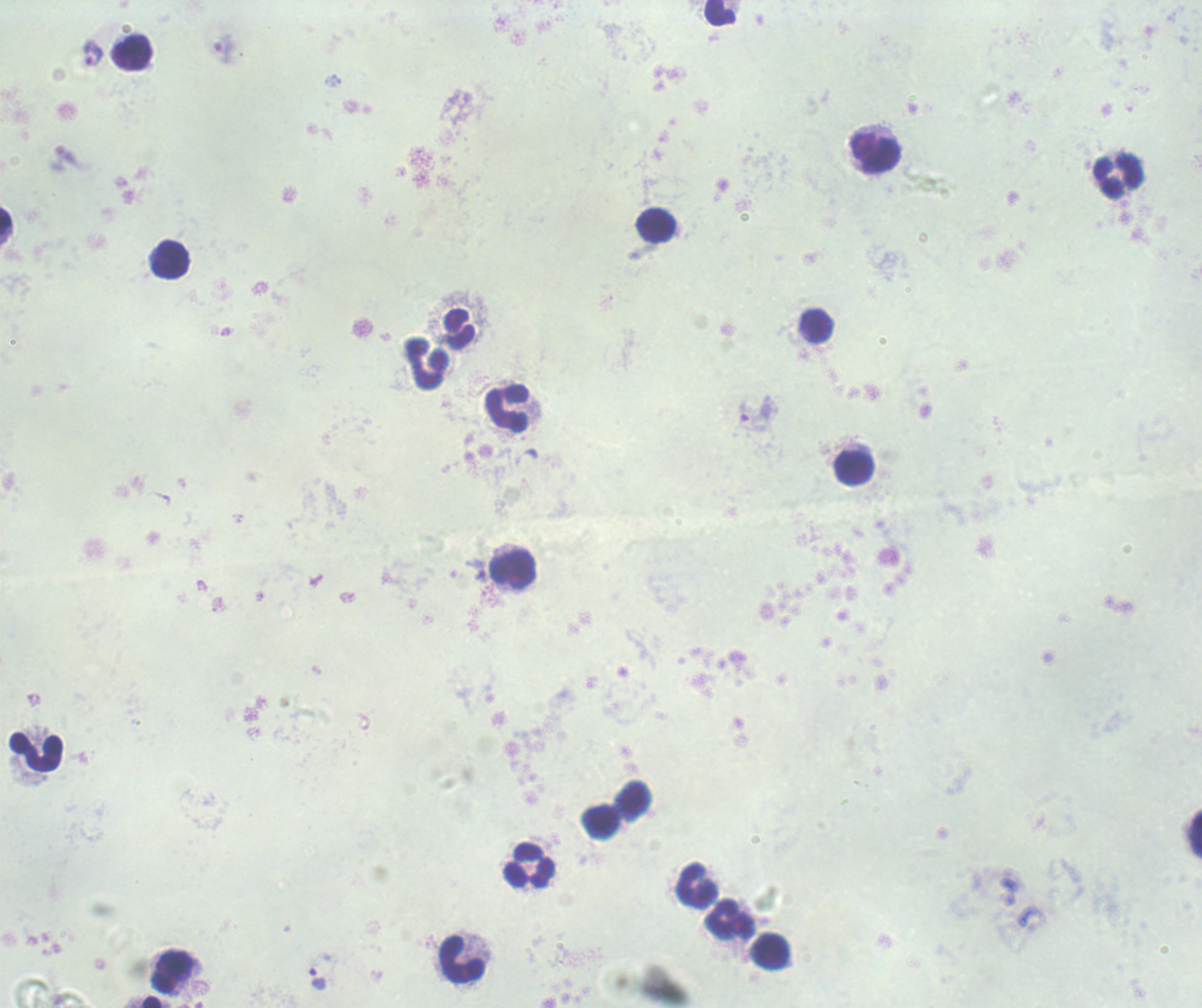 Approximate object centers, in pixels from the top-left corner. Trophozoite locations: (x=225, y=50), (x=91, y=54), (x=67, y=156), (x=744, y=412), (x=481, y=577), (x=318, y=979). Leukocyte locations: (x=719, y=13), (x=131, y=53), (x=875, y=153), (x=1118, y=176), (x=5, y=220), (x=656, y=225), (x=170, y=259), (x=817, y=325), (x=459, y=328), (x=427, y=364), (x=507, y=407), (x=854, y=469), (x=513, y=570), (x=35, y=752), (x=633, y=800), (x=601, y=821), (x=1196, y=833), (x=529, y=865), (x=697, y=885), (x=731, y=920), (x=770, y=952), (x=462, y=959), (x=173, y=973), (x=152, y=1002). Image is 1202×1008 pixels. Romanowsky-stained preparation. Background quality: poor. Captured at 100x magnification. Result: positive for malaria parasites. Thick smear of blood. One field from this slide. Previously used in a real diagnosis.